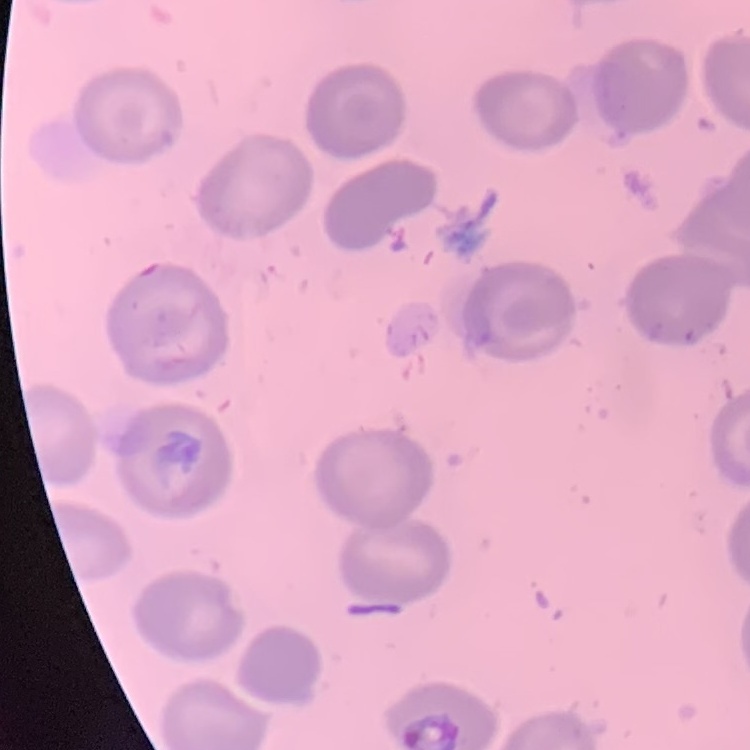
{
  "red_blood_cell_morphology": "no rouleaux formation",
  "image_type": "square crop of a larger photomicrograph",
  "preparation": "thin blood film",
  "stain": "Field's or Giemsa"
}